Classify this cell by malaria status.
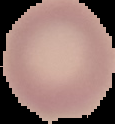

It is uninfected.

Image is 115×124 pixels. Segmented cell region on a black background. From a thin blood film.